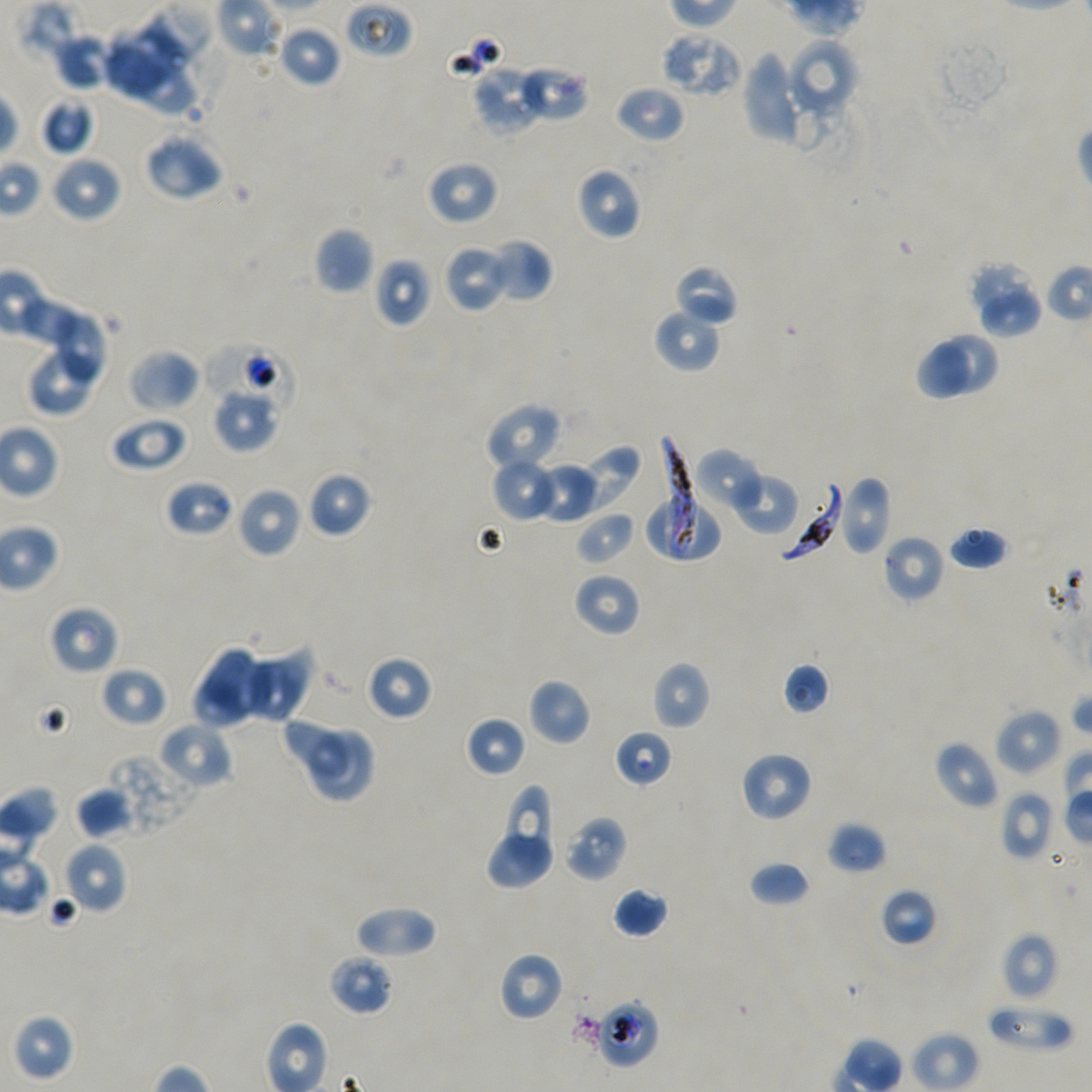

Approximate bounding boxes as (x1, y1, x2, y2) in pixels. Not every red blood cell is marked.
Summary:
  - Locations of uninfected red blood cells: (277, 24, 343, 88), (659, 32, 743, 98), (52, 33, 116, 90), (786, 38, 858, 115), (103, 41, 173, 95), (742, 51, 812, 146), (134, 62, 197, 114), (472, 65, 546, 134), (517, 65, 590, 124), (613, 85, 685, 144), (39, 98, 94, 155), (143, 132, 224, 201), (50, 154, 122, 223), (426, 159, 498, 225), (576, 167, 641, 240), (314, 228, 375, 295), (488, 239, 553, 302), (442, 244, 511, 313), (373, 257, 434, 327), (967, 261, 1033, 315), (673, 264, 740, 327), (981, 290, 1044, 337), (22, 294, 78, 348), (653, 307, 722, 374), (54, 314, 105, 382), (939, 331, 1000, 393), (915, 341, 971, 402), (128, 349, 201, 413), (29, 352, 94, 413), (213, 389, 279, 452), (484, 403, 562, 472), (109, 414, 188, 473), (571, 441, 643, 515), (693, 449, 766, 514), (491, 456, 558, 523), (533, 462, 599, 525), (729, 469, 799, 536), (307, 471, 372, 538), (838, 475, 893, 555), (236, 486, 303, 559), (647, 499, 722, 561), (575, 511, 636, 566), (947, 525, 1011, 570), (881, 534, 945, 603), (573, 572, 640, 637), (49, 604, 119, 675), (243, 649, 312, 722), (202, 651, 271, 716), (365, 655, 433, 722), (651, 661, 711, 730), (782, 661, 831, 715), (100, 666, 166, 727), (528, 678, 592, 746), (192, 689, 247, 728), (994, 707, 1062, 776), (465, 715, 527, 778), (286, 718, 349, 782), (157, 721, 234, 790), (311, 730, 371, 799), (933, 740, 998, 810), (739, 750, 813, 822), (99, 754, 198, 837), (74, 786, 133, 839), (506, 788, 547, 868), (999, 790, 1055, 862), (564, 814, 627, 881), (827, 822, 887, 875), (488, 835, 551, 888), (62, 841, 128, 914), (748, 861, 811, 907), (613, 887, 669, 938), (880, 888, 938, 947), (353, 905, 437, 960), (1000, 932, 1059, 1000), (498, 951, 564, 1022), (327, 953, 395, 1016), (986, 1001, 1074, 1052), (14, 1014, 74, 1080)
  - Locations of red blood cells of indeterminate infection status: (346, 1, 415, 59), (204, 344, 295, 414), (164, 478, 234, 538), (614, 729, 673, 788), (591, 998, 660, 1068)
  - Locations of infected red blood cells: (660, 437, 696, 560), (779, 482, 844, 562)
  - Image size: 1092×1092 pixels
  - Donor blood group: A+/O+
  - Stain: Giemsa
  - Preparation: thin blood film
  - Objective: 100x, oil immersion, numerical aperture 1.45
  - Field of view: one from this slide
  - Culture: in-vitro P. falciparum strain NF54, static